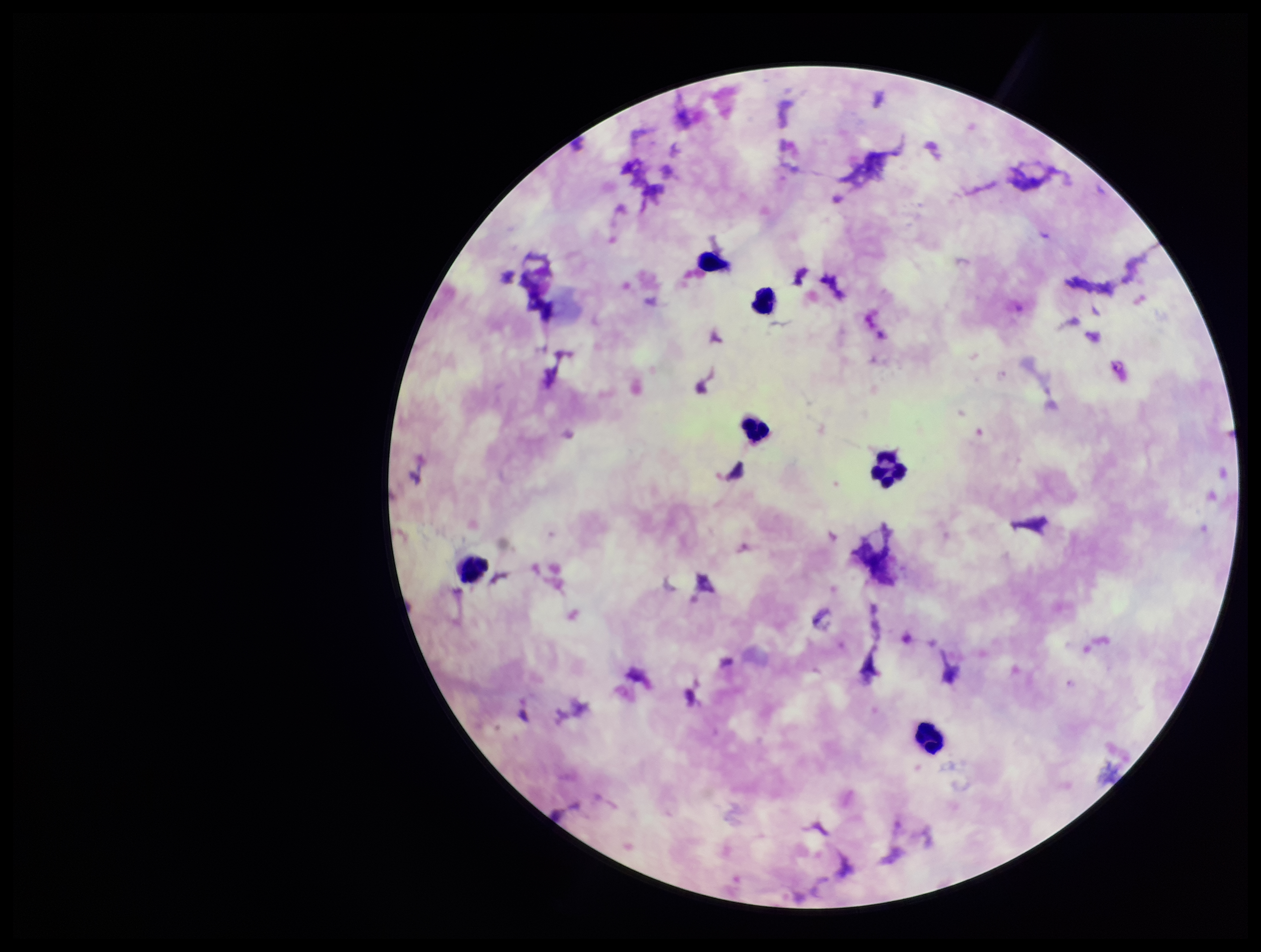

Plasmodium parasites = identified
leukocyte count = 6
parasite count = 1
preparation = thick blood smear
field of view = one from this slide
capture = smartphone photograph through the microscope eyepiece
patient malaria status = infected
stain = Giemsa
image size = 1261×952 pixels
species reported for this patient = Plasmodium falciparum